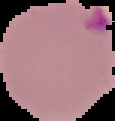

Summary:
  - Preparation: thin blood smear
  - Result: malaria parasites detected
  - Image size: 115×121 pixels
  - Image type: cell region segmented out of the field of view; surrounding area masked to black